Name the parasite shown.
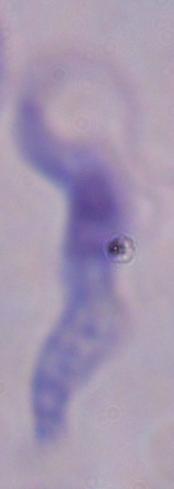
This is a trypanosome.

Captured at 1000x magnification. Photomicrograph.